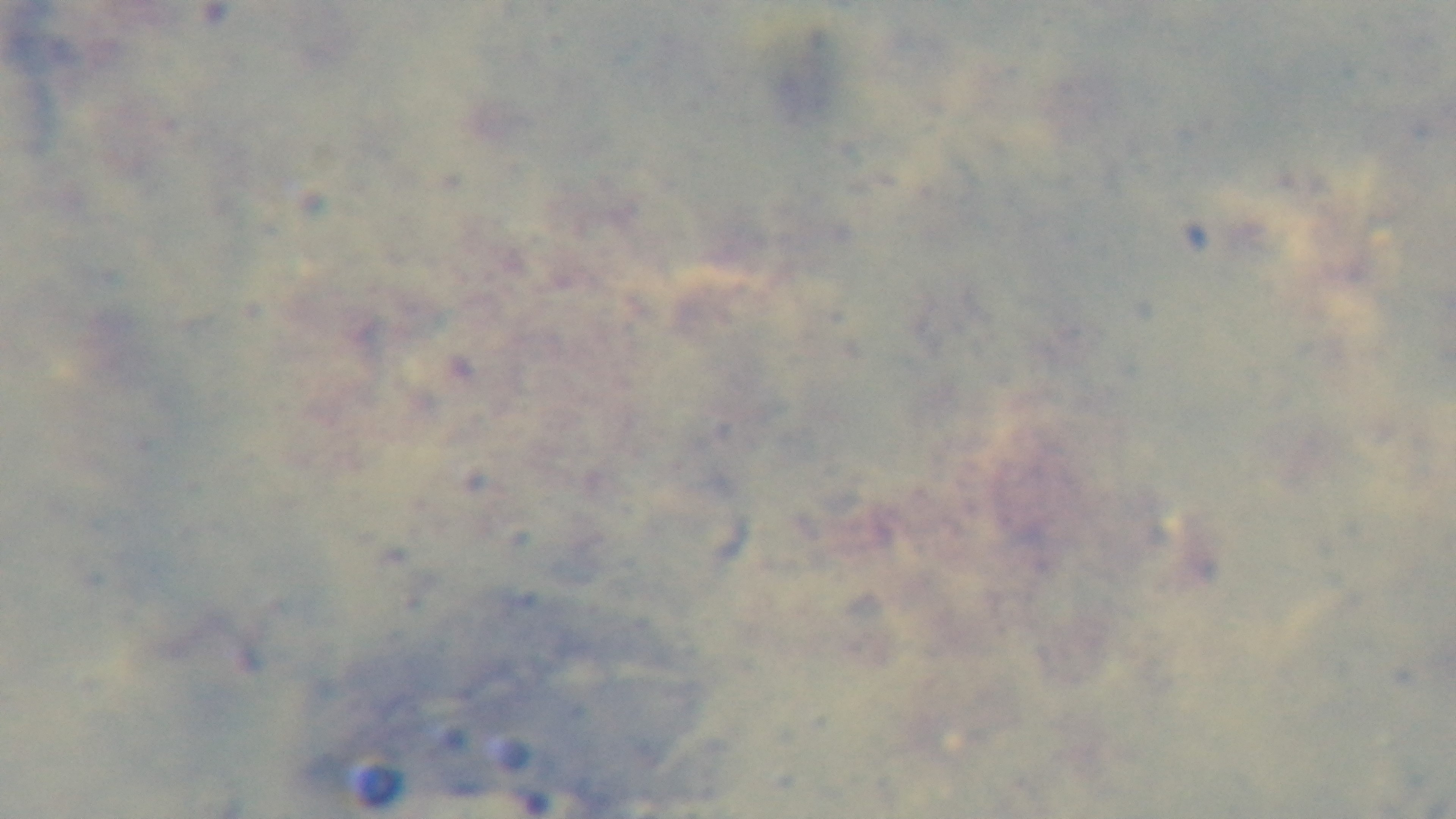
Summary:
  - Capture: mounted 4K digital camera
  - Stain: Giemsa
  - Field of view: single
  - Modality: light microscopy
  - Preparation: thick smear
  - Objective: 100x oil immersion
  - Malaria status: negative